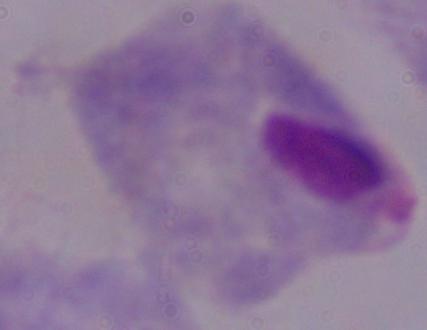
1000x magnification. Micrograph. A trichomonad is seen.